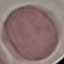 Result: no malaria parasites detected. Acquired by smartphone through the microscope eyepiece. Thin blood smear. Giemsa stain. Cell patch, automatically extracted from a larger field of view and resized to 64 × 64 pixels.